Describe the morphology of the erythrocytes.
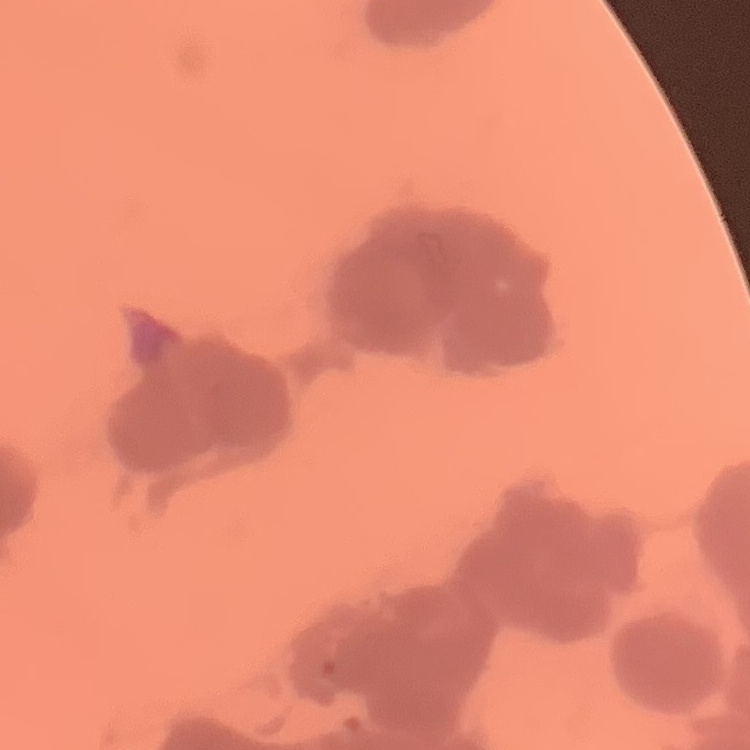

They show rouleaux formation.

image type = one tile cut from a larger photomicrograph
stain = Field's or Giemsa
preparation = thin peripheral smear